State the blood parasite species.
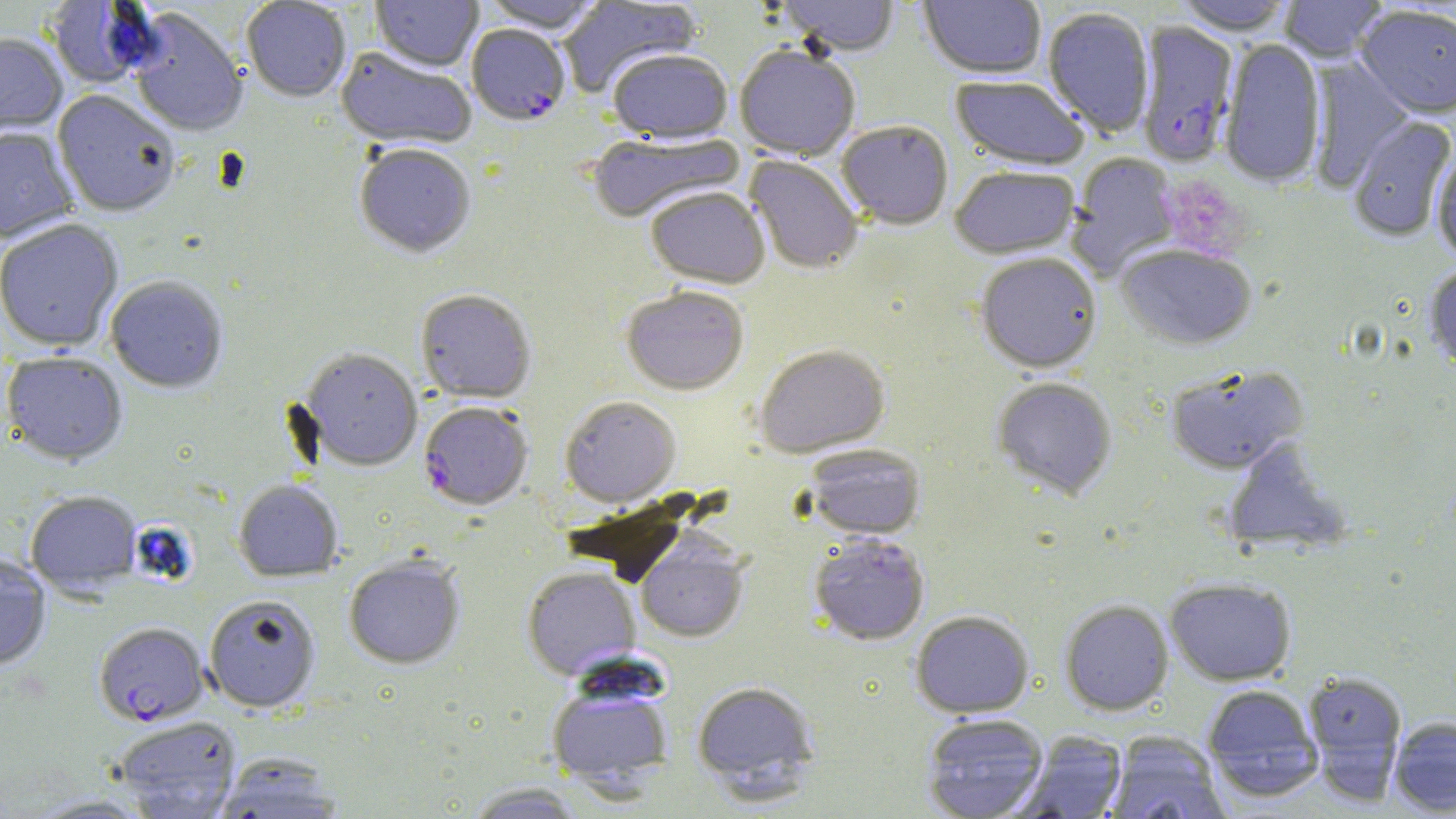

Plasmodium falciparum.

platelet locations = approximate bounding boxes as [x1, y1, x2, y2] in pixels: [1164, 176, 1250, 258]
preparation = thin blood smear
field of view = single
magnification = 1000x
image size = 1456×819 pixels
uninfected red blood cell locations = approximate bounding boxes as [x1, y1, x2, y2] in pixels: [241, 0, 351, 104], [371, 0, 482, 73], [479, 0, 606, 35], [558, 0, 702, 98], [777, 0, 900, 59], [919, 0, 1046, 81], [1174, 0, 1296, 38], [1278, 0, 1388, 65], [43, 1, 159, 90], [1355, 7, 1456, 122], [127, 9, 247, 139], [1043, 9, 1154, 139], [0, 34, 67, 141], [1219, 40, 1325, 188], [734, 47, 860, 161], [335, 48, 476, 152], [607, 51, 734, 145], [1308, 60, 1414, 191], [949, 77, 1088, 171], [52, 91, 180, 218], [1348, 116, 1455, 243], [837, 123, 953, 231], [0, 128, 78, 244], [586, 131, 745, 224], [354, 145, 476, 260], [1431, 149, 1456, 265], [1067, 152, 1181, 279], [745, 156, 863, 275], [950, 167, 1080, 259], [645, 189, 770, 290], [0, 220, 124, 353], [1116, 244, 1257, 351], [975, 254, 1102, 375], [1424, 265, 1456, 377], [106, 277, 228, 394], [621, 288, 749, 396], [415, 290, 537, 404], [753, 346, 890, 458], [299, 349, 423, 471], [2, 353, 128, 467], [1165, 366, 1308, 476], [991, 379, 1117, 502], [560, 396, 682, 508], [1221, 442, 1352, 556], [803, 445, 925, 540], [233, 480, 343, 582], [26, 492, 142, 596], [809, 534, 930, 646], [635, 535, 749, 643], [0, 556, 51, 670], [343, 556, 466, 670], [522, 567, 640, 680], [1164, 577, 1297, 686], [204, 595, 321, 712], [1060, 599, 1174, 715], [910, 610, 1034, 717], [1303, 671, 1408, 793], [545, 677, 675, 793], [691, 680, 820, 798], [1201, 684, 1323, 800], [921, 713, 1048, 819], [112, 716, 242, 818], [1388, 716, 1456, 815], [1016, 731, 1127, 818], [1105, 732, 1229, 819], [211, 754, 346, 819], [462, 782, 591, 818], [27, 794, 156, 818]
Plasmodium falciparum-infected red blood cell locations = approximate bounding boxes as [x1, y1, x2, y2] in pixels: [1135, 22, 1240, 168], [467, 25, 571, 127], [419, 401, 533, 510], [94, 622, 209, 726]
modality = light microscopy
stain = May-Grünwald-Giemsa